Assess this cell for malaria.
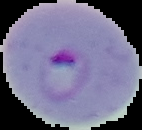

Parasitized.

Summary:
  - Preparation: thin blood film
  - Image size: 142×130 pixels
  - Image type: cell region segmented out of the field of view; surrounding area masked to black